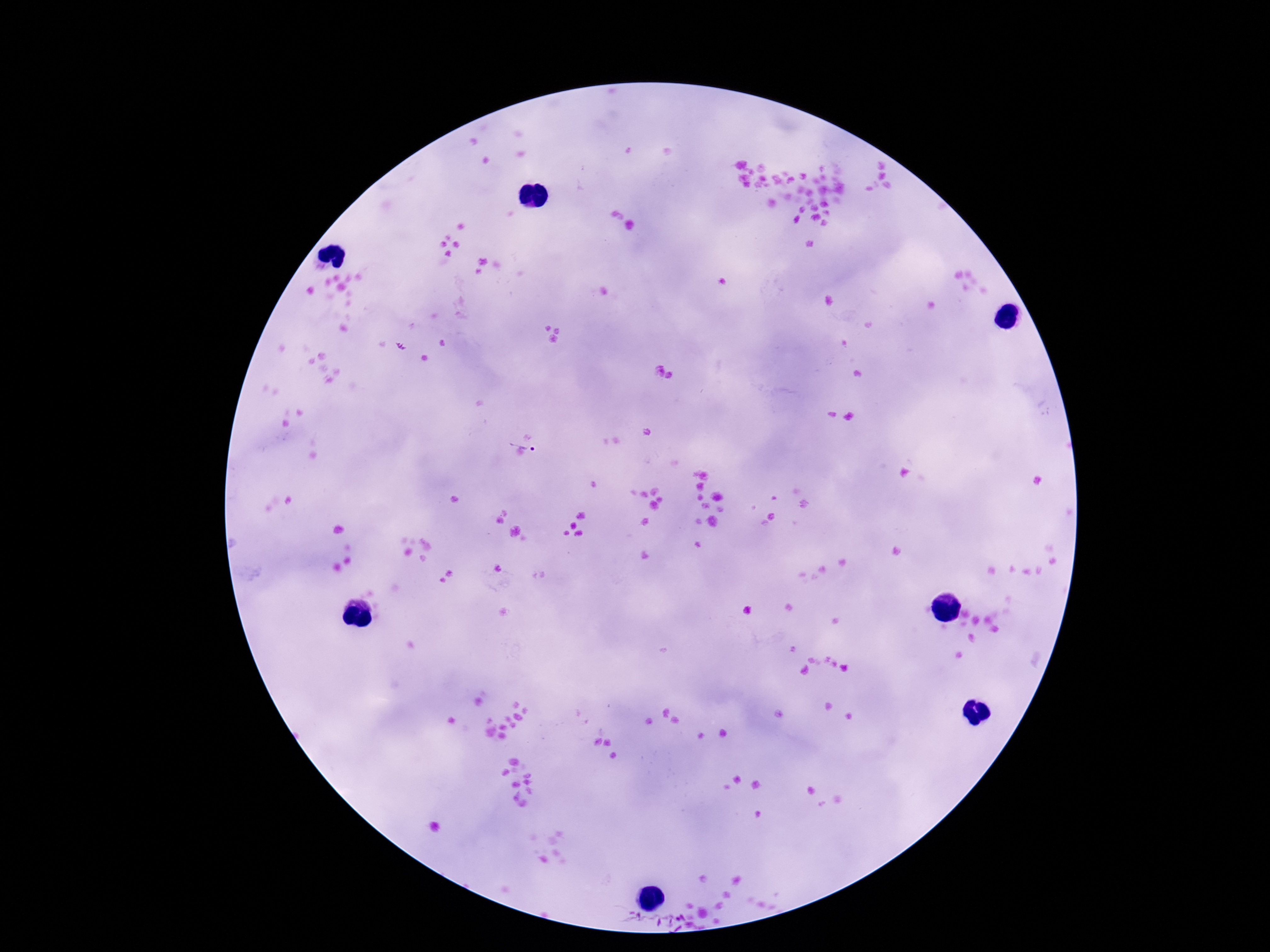
Approximate centers as {x, y} in pixels.
Summary:
  - Plasmodium parasite locations: {521, 447}
  - Stain: Giemsa
  - Field of view: single
  - Capture: smartphone camera through the microscope eyepiece
  - Preparation: thick blood film
  - Image size: 1270×952 pixels
  - Patient malaria status: positive
  - Magnification: 100x